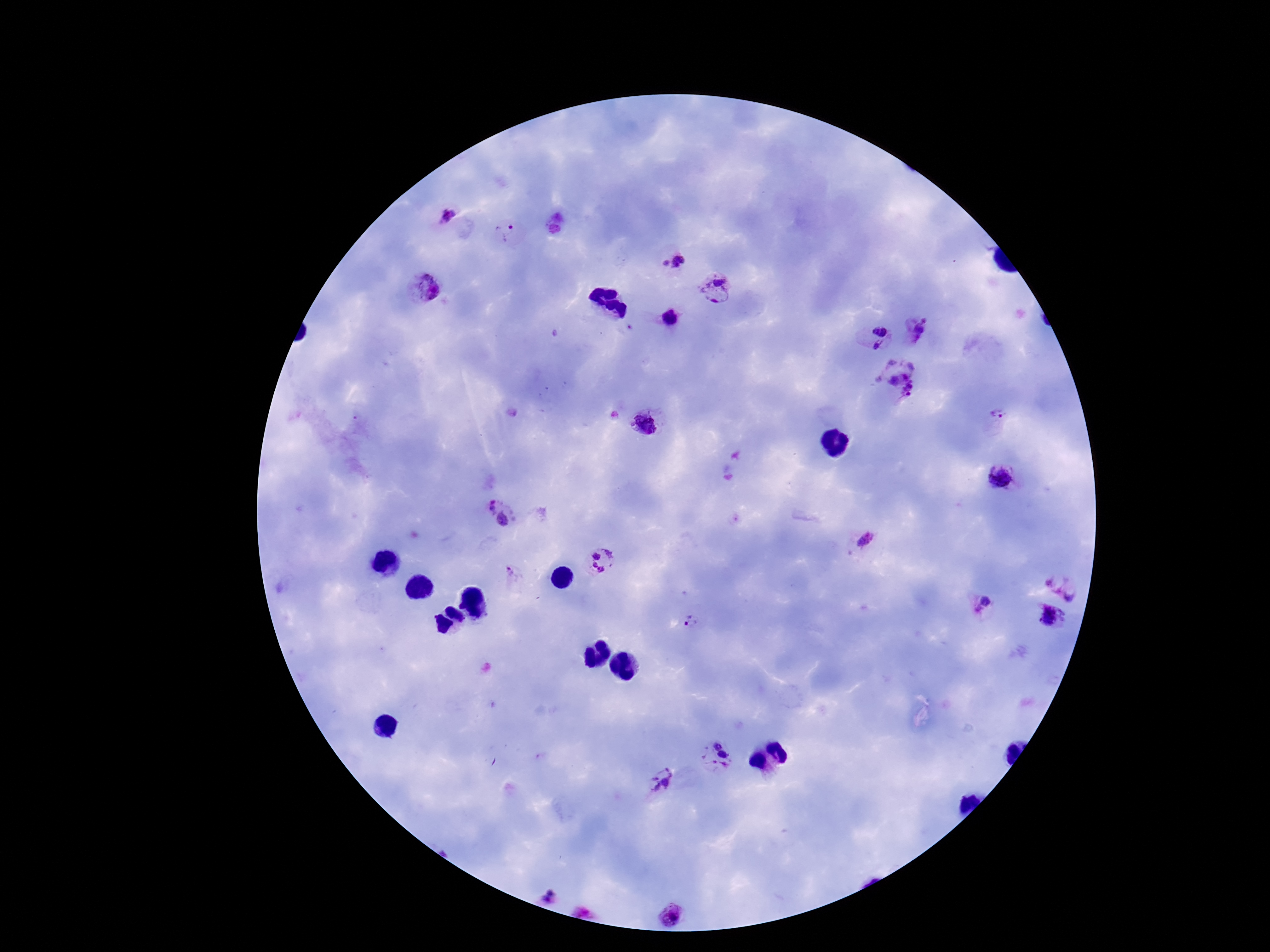

{
  "preparation": "thick blood smear",
  "capture": "smartphone camera through the microscope eyepiece",
  "patient_malaria_status": "infected",
  "image_size": "1270×952 pixels",
  "magnification": "100x",
  "field_of_view": "single",
  "plasmodium_parasite_locations": "approximate centers as (x, y) in pixels: (446, 215), (506, 232), (672, 260), (714, 289), (425, 292), (671, 318), (919, 330), (877, 337), (903, 379), (999, 419), (650, 422), (1002, 478), (499, 513), (865, 541), (601, 561), (510, 573), (1068, 579), (985, 603), (1055, 616), (693, 620), (718, 756), (659, 781), (551, 895), (675, 914)",
  "stain": "Giemsa"
}